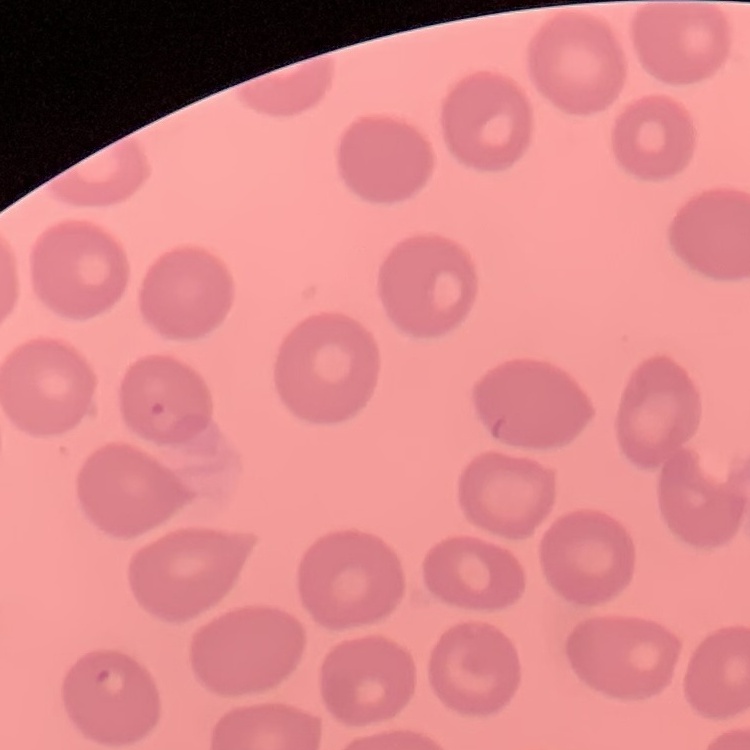
red_blood_cell_morphology: no rouleaux formation
image_type: square crop of a larger photomicrograph
preparation: thin peripheral smear
stain: Field's or Giemsa